Give the preparation type.
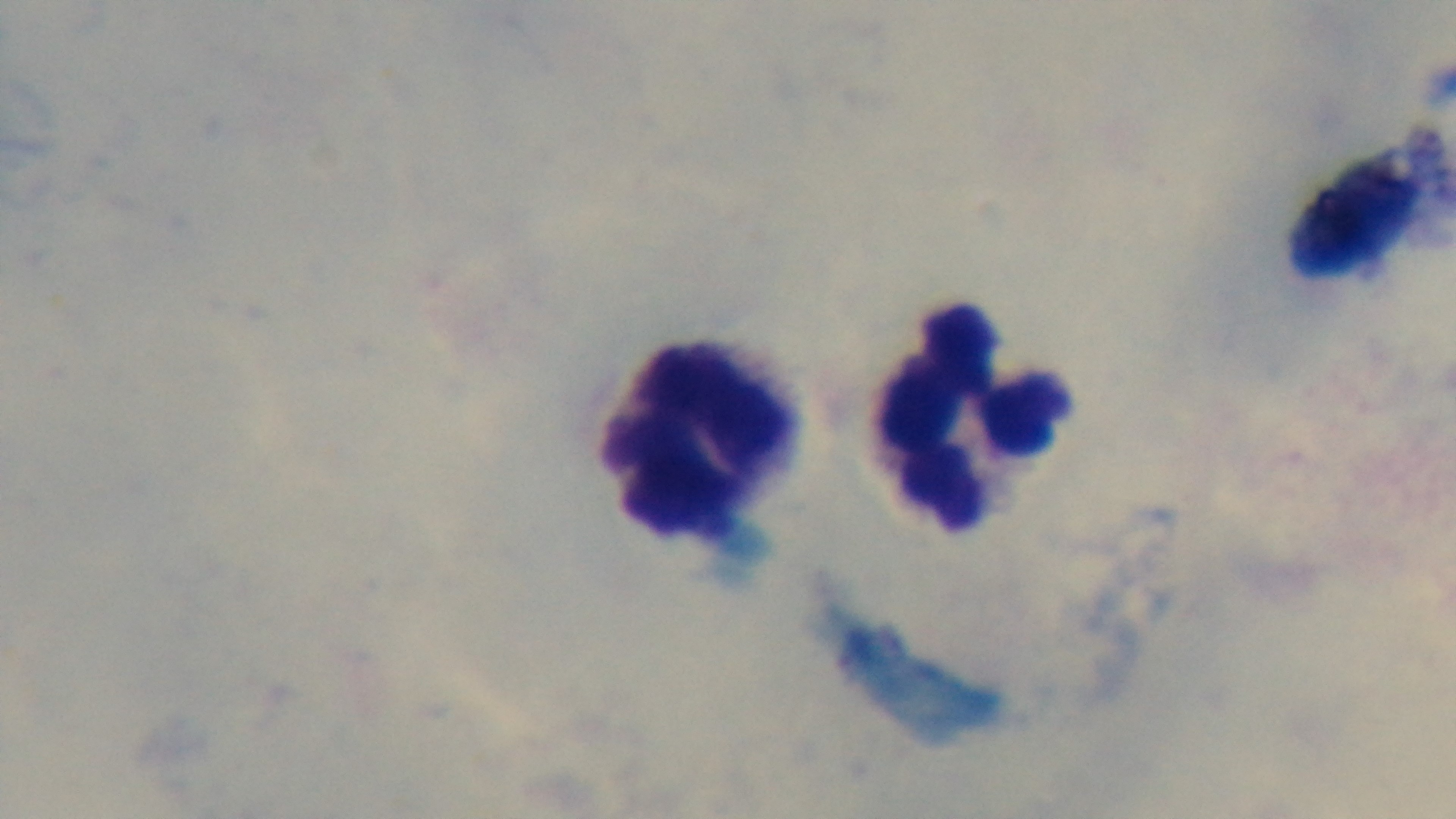

It is a thick blood film.

Photomicrograph. Malaria status: negative. Giemsa stain. Mounted 4K digital camera. Single field of view. 100x oil-immersion objective.